Report the malaria status of this cell.
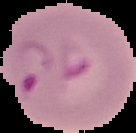

Parasitized.

image_type: segmented cell region on a black background
preparation: thin blood film
image_size: 136×133 pixels